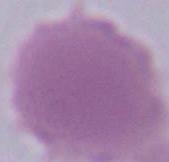

Captured at 1000x magnification. An erythrocyte is shown. Photomicrograph.